Assess this cell for malaria.
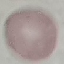

It is uninfected.

Thin smear of blood. Automatically extracted cell patch, resized to 64 × 64 pixels. Photographed with a smartphone camera at the microscope eyepiece. Giemsa-stained preparation.